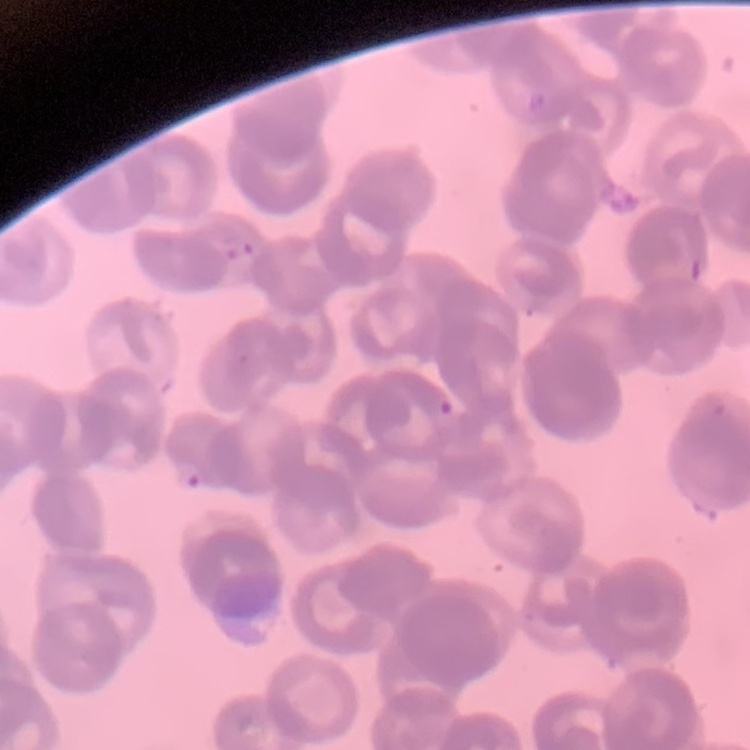
The erythrocytes show rouleaux formation. Square crop of a larger photomicrograph. Thin blood smear. Field's or Giemsa stain.